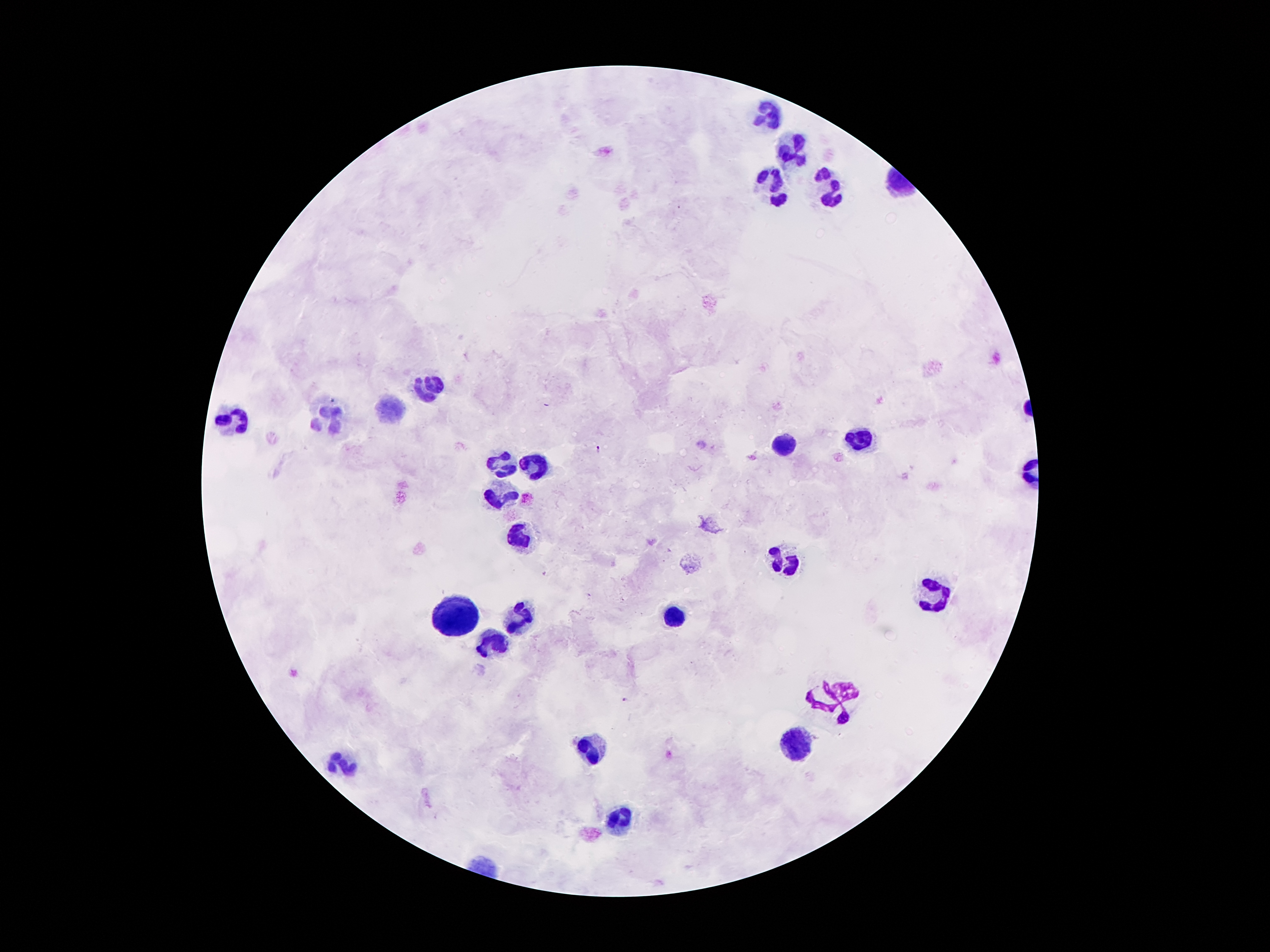
Approximate centers as [x, y] in pixels. Leukocyte locations: [766, 115], [792, 148], [827, 185], [769, 187], [433, 386], [393, 410], [228, 421], [328, 424], [858, 439], [781, 446], [501, 465], [531, 465], [500, 498], [519, 539], [781, 559], [935, 595], [459, 614], [519, 615], [671, 616], [494, 641], [832, 700], [797, 746], [589, 748], [344, 762], [622, 814]. Plasmodium parasite locations: [600, 450], [627, 699]. Single field of view. 100x magnification. Thick peripheral-blood smear. Photographed through the microscope eyepiece with a smartphone camera. Image is 1270×952 pixels. Giemsa-stained preparation. Patient malaria status: positive for Plasmodium falciparum.